Classify this cell by malaria status.
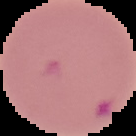
It is parasitized.

preparation: thin blood smear
image_type: cell region segmented out of the field of view; surrounding area masked to black
image_size: 136×136 pixels